State the preparation type.
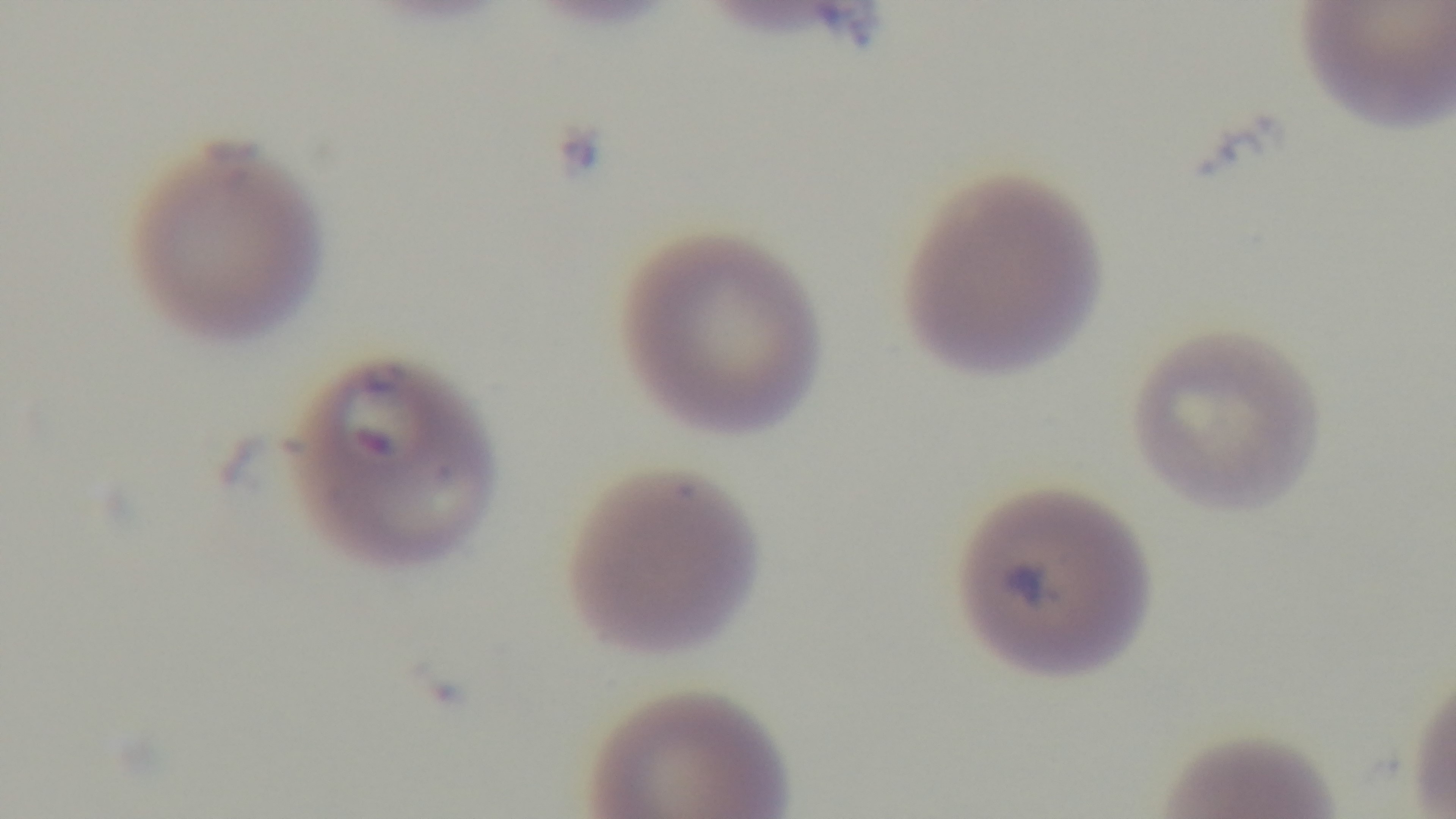
A thin smear.

Summary:
  - Capture: mounted 4K digital camera
  - Malaria status: infected
  - Stain: Giemsa
  - Objective: 100x oil immersion
  - Modality: light microscopy
  - Field of view: single